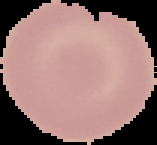 Image is 157×145 pixels. From a thin blood film. Cell region segmented out of the field of view; the surrounding area is masked to black. Result: no malaria parasites detected.